State which parasite is depicted.
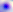

This is Toxoplasma gondii.

{
  "modality": "photomicrograph",
  "magnification": "400x"
}